Identify the blood parasite species.
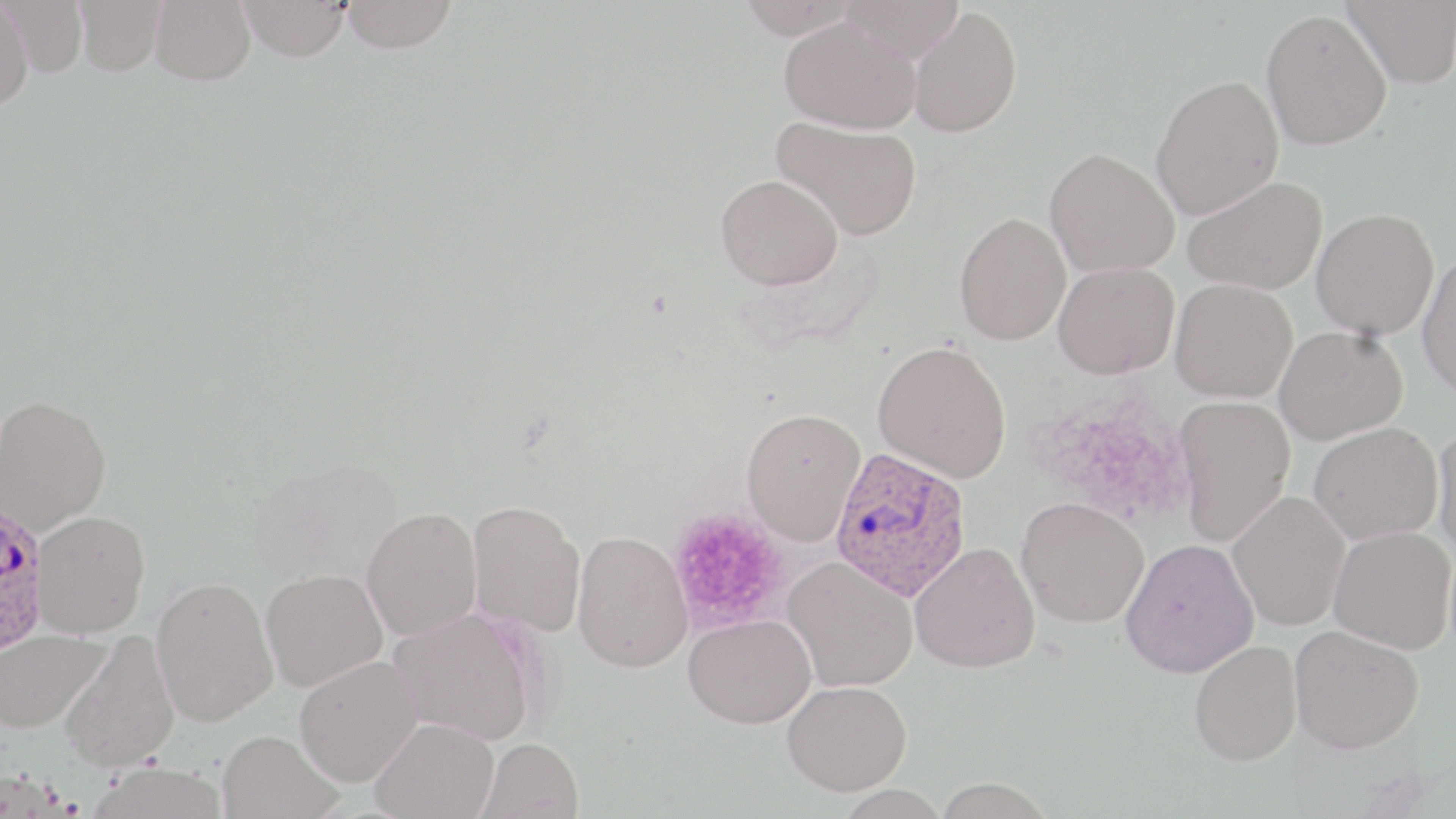
Plasmodium ovale.

Approximate bounding boxes as named x1/y1/x2/y2 corners in pixels. Plasmodium ovale-infected red blood cell locations: (x1=829, y1=446, x2=971, y2=601), (x1=1, y1=509, x2=54, y2=658). Platelet locations: (x1=1034, y1=392, x2=1193, y2=526), (x1=667, y1=507, x2=791, y2=633). Uninfected red blood cell locations: (x1=2, y1=0, x2=87, y2=76), (x1=74, y1=0, x2=166, y2=75), (x1=150, y1=0, x2=255, y2=85), (x1=341, y1=0, x2=457, y2=53), (x1=735, y1=0, x2=863, y2=39), (x1=837, y1=0, x2=965, y2=62), (x1=1342, y1=0, x2=1456, y2=88), (x1=239, y1=1, x2=351, y2=61), (x1=0, y1=2, x2=33, y2=111), (x1=909, y1=6, x2=1022, y2=137), (x1=1261, y1=9, x2=1391, y2=150), (x1=779, y1=17, x2=922, y2=134), (x1=1150, y1=75, x2=1283, y2=220), (x1=771, y1=117, x2=922, y2=240), (x1=1045, y1=148, x2=1179, y2=278), (x1=715, y1=174, x2=844, y2=290), (x1=1183, y1=175, x2=1327, y2=295), (x1=1311, y1=208, x2=1439, y2=339), (x1=953, y1=212, x2=1071, y2=345), (x1=1416, y1=252, x2=1456, y2=399), (x1=1053, y1=261, x2=1179, y2=379), (x1=1170, y1=278, x2=1297, y2=401), (x1=1275, y1=325, x2=1407, y2=443), (x1=872, y1=339, x2=1012, y2=483), (x1=0, y1=394, x2=112, y2=533), (x1=1173, y1=395, x2=1296, y2=547), (x1=741, y1=407, x2=866, y2=546), (x1=1432, y1=422, x2=1456, y2=560), (x1=1309, y1=423, x2=1442, y2=544), (x1=1227, y1=491, x2=1350, y2=631), (x1=1017, y1=496, x2=1149, y2=627), (x1=467, y1=499, x2=587, y2=637), (x1=361, y1=505, x2=483, y2=641), (x1=33, y1=510, x2=150, y2=637), (x1=1329, y1=526, x2=1455, y2=654), (x1=572, y1=530, x2=692, y2=673), (x1=1120, y1=538, x2=1260, y2=678), (x1=910, y1=541, x2=1041, y2=673), (x1=782, y1=556, x2=918, y2=692), (x1=260, y1=569, x2=387, y2=692), (x1=151, y1=577, x2=278, y2=726), (x1=389, y1=608, x2=538, y2=745), (x1=684, y1=613, x2=816, y2=728), (x1=1289, y1=624, x2=1423, y2=754), (x1=0, y1=629, x2=110, y2=733), (x1=59, y1=630, x2=180, y2=772), (x1=1189, y1=640, x2=1301, y2=765), (x1=295, y1=655, x2=422, y2=787), (x1=782, y1=680, x2=912, y2=795), (x1=370, y1=717, x2=498, y2=819), (x1=218, y1=730, x2=342, y2=819), (x1=477, y1=738, x2=584, y2=819), (x1=86, y1=761, x2=229, y2=819). Thin blood smear. Image is 1456×819 pixels. Optical microscopy. May-Grünwald-Giemsa stain. 1000x magnification. One field of a larger specimen.